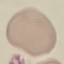 Malaria status: uninfected. Thin blood smear. Cell patch, automatically extracted from a larger field of view and resized to 64 × 64 pixels. Photographed with a smartphone camera at the microscope eyepiece. Giemsa-stained preparation.